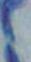
{
  "magnification": "1000x",
  "identification": "Toxoplasma gondii",
  "modality": "micrograph"
}